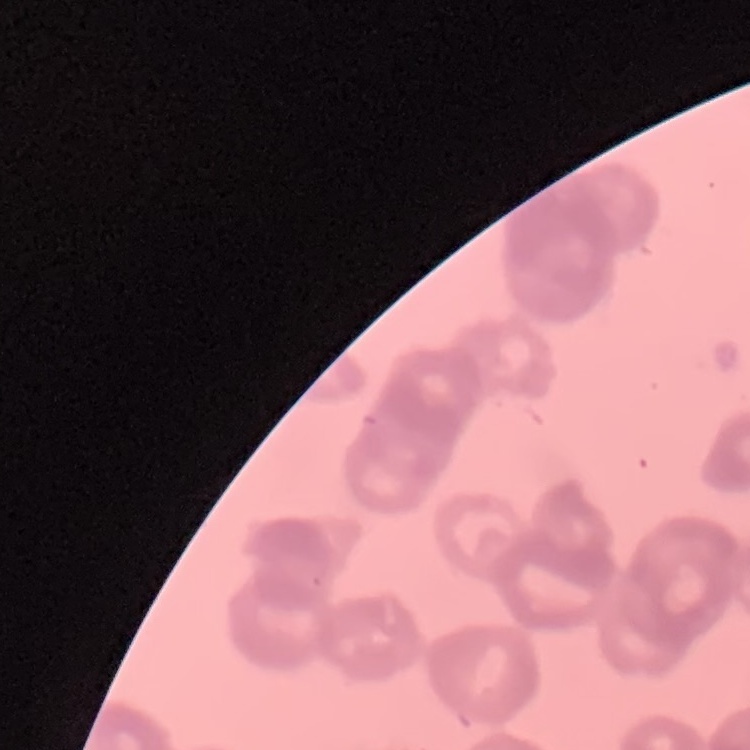

The erythrocytes show rouleaux formation. Stained with either Field's or Giemsa. One tile cut from a larger photomicrograph. Thin peripheral smear.